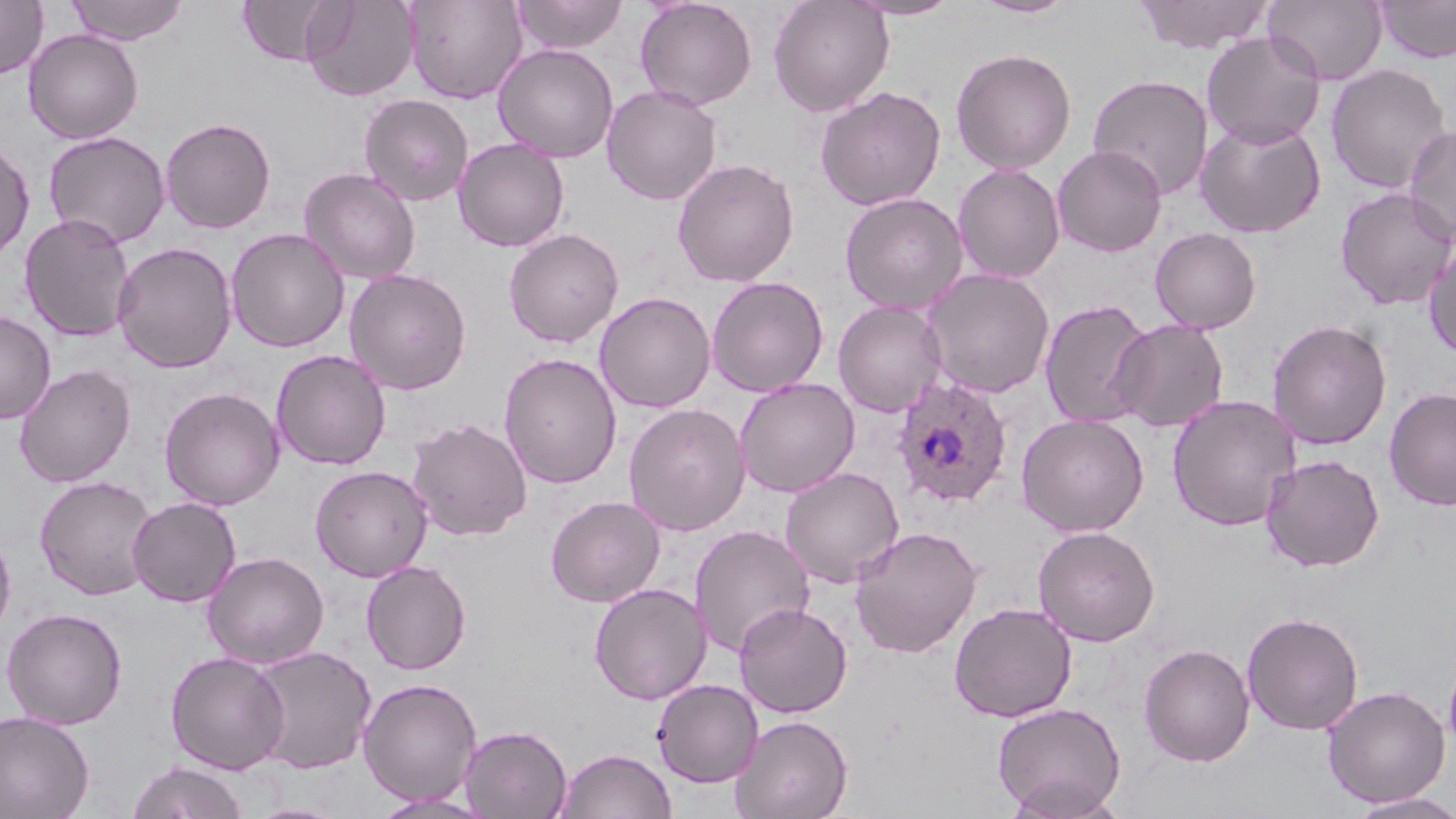

Approximate bounding boxes as named x1/y1/x2/y2 corners in pixels. Plasmodium ovale-infected red blood cell locations: (x1=890, y1=375, x2=1014, y2=509). Uninfected red blood cell locations: (x1=0, y1=0, x2=48, y2=78), (x1=65, y1=0, x2=189, y2=45), (x1=237, y1=0, x2=343, y2=67), (x1=302, y1=0, x2=419, y2=101), (x1=404, y1=0, x2=527, y2=104), (x1=512, y1=0, x2=628, y2=55), (x1=635, y1=0, x2=758, y2=110), (x1=768, y1=0, x2=894, y2=116), (x1=845, y1=0, x2=964, y2=20), (x1=970, y1=0, x2=1079, y2=19), (x1=1135, y1=0, x2=1275, y2=53), (x1=1263, y1=0, x2=1388, y2=85), (x1=1375, y1=0, x2=1456, y2=63), (x1=23, y1=29, x2=144, y2=144), (x1=1202, y1=31, x2=1326, y2=149), (x1=493, y1=43, x2=619, y2=163), (x1=951, y1=48, x2=1076, y2=174), (x1=1326, y1=63, x2=1451, y2=194), (x1=1087, y1=73, x2=1214, y2=200), (x1=602, y1=84, x2=722, y2=205), (x1=815, y1=86, x2=946, y2=211), (x1=359, y1=94, x2=474, y2=206), (x1=1195, y1=116, x2=1326, y2=239), (x1=160, y1=117, x2=276, y2=234), (x1=1403, y1=123, x2=1456, y2=246), (x1=43, y1=131, x2=170, y2=248), (x1=0, y1=137, x2=36, y2=261), (x1=453, y1=137, x2=570, y2=252), (x1=1052, y1=145, x2=1167, y2=257), (x1=672, y1=158, x2=799, y2=287), (x1=952, y1=163, x2=1065, y2=283), (x1=299, y1=167, x2=420, y2=284), (x1=1334, y1=187, x2=1456, y2=311), (x1=840, y1=192, x2=968, y2=314), (x1=18, y1=213, x2=136, y2=342), (x1=226, y1=227, x2=350, y2=353), (x1=1150, y1=227, x2=1261, y2=334), (x1=504, y1=228, x2=624, y2=347), (x1=1423, y1=239, x2=1456, y2=360), (x1=113, y1=241, x2=238, y2=373), (x1=921, y1=267, x2=1056, y2=399), (x1=344, y1=268, x2=472, y2=395), (x1=706, y1=275, x2=829, y2=398), (x1=595, y1=291, x2=716, y2=414), (x1=1039, y1=298, x2=1156, y2=429), (x1=833, y1=299, x2=947, y2=417), (x1=0, y1=311, x2=56, y2=423), (x1=1267, y1=318, x2=1393, y2=451), (x1=1111, y1=319, x2=1229, y2=432), (x1=271, y1=349, x2=391, y2=470), (x1=498, y1=352, x2=622, y2=490), (x1=14, y1=364, x2=136, y2=487), (x1=734, y1=377, x2=860, y2=498), (x1=159, y1=386, x2=285, y2=511), (x1=1384, y1=387, x2=1456, y2=510), (x1=1167, y1=394, x2=1301, y2=531), (x1=623, y1=403, x2=752, y2=536), (x1=1016, y1=413, x2=1149, y2=537), (x1=407, y1=418, x2=532, y2=541), (x1=1260, y1=454, x2=1384, y2=572), (x1=310, y1=464, x2=434, y2=581), (x1=780, y1=467, x2=905, y2=588), (x1=35, y1=475, x2=157, y2=600), (x1=545, y1=495, x2=666, y2=608), (x1=127, y1=496, x2=241, y2=607), (x1=689, y1=524, x2=815, y2=658), (x1=849, y1=525, x2=982, y2=658), (x1=1032, y1=525, x2=1160, y2=646), (x1=0, y1=526, x2=16, y2=644), (x1=202, y1=551, x2=329, y2=668), (x1=361, y1=560, x2=472, y2=674), (x1=589, y1=582, x2=712, y2=705), (x1=734, y1=602, x2=853, y2=718), (x1=949, y1=602, x2=1077, y2=723), (x1=1, y1=607, x2=128, y2=729), (x1=1241, y1=611, x2=1364, y2=735), (x1=1139, y1=643, x2=1255, y2=766), (x1=247, y1=645, x2=377, y2=774), (x1=1443, y1=649, x2=1456, y2=760), (x1=165, y1=651, x2=290, y2=774), (x1=358, y1=678, x2=483, y2=805), (x1=652, y1=679, x2=764, y2=788), (x1=1322, y1=685, x2=1450, y2=808), (x1=992, y1=701, x2=1126, y2=816), (x1=0, y1=710, x2=95, y2=819), (x1=731, y1=714, x2=852, y2=819), (x1=459, y1=724, x2=572, y2=819), (x1=557, y1=747, x2=676, y2=819), (x1=127, y1=760, x2=249, y2=819), (x1=1003, y1=776, x2=1125, y2=819), (x1=370, y1=792, x2=497, y2=818), (x1=1346, y1=793, x2=1456, y2=818), (x1=248, y1=802, x2=348, y2=819). Slide-level diagnosis: Plasmodium ovale. Optical microscopy. One field of a larger specimen. Thin blood film. Captured at 1000x magnification. May-Grünwald-Giemsa stain. Image is 1456×819 pixels.